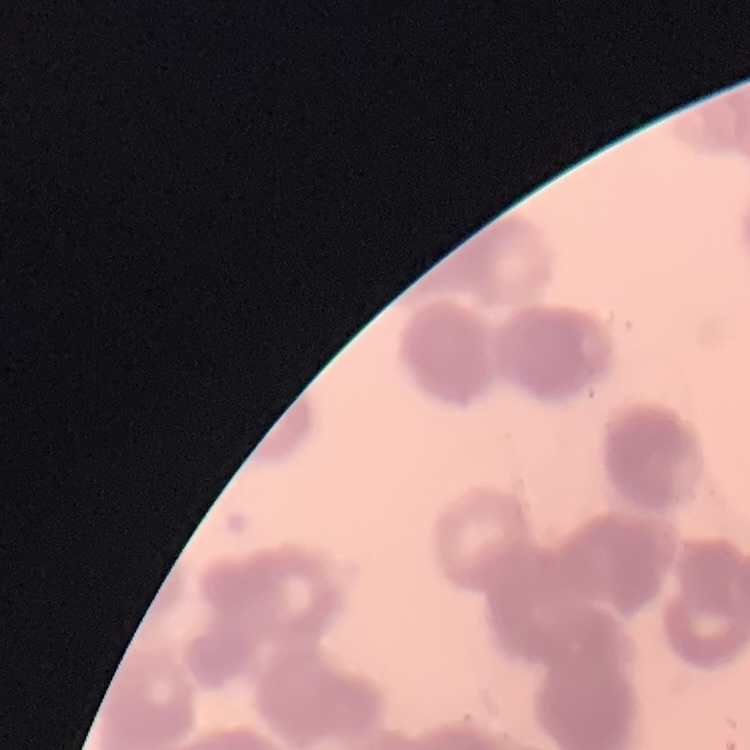

Summary:
  - Red blood cell morphology: rouleaux formation
  - Image type: square crop of a larger photomicrograph
  - Preparation: thin blood smear
  - Stain: Field's or Giemsa